Locate every uninfected red blood cell.
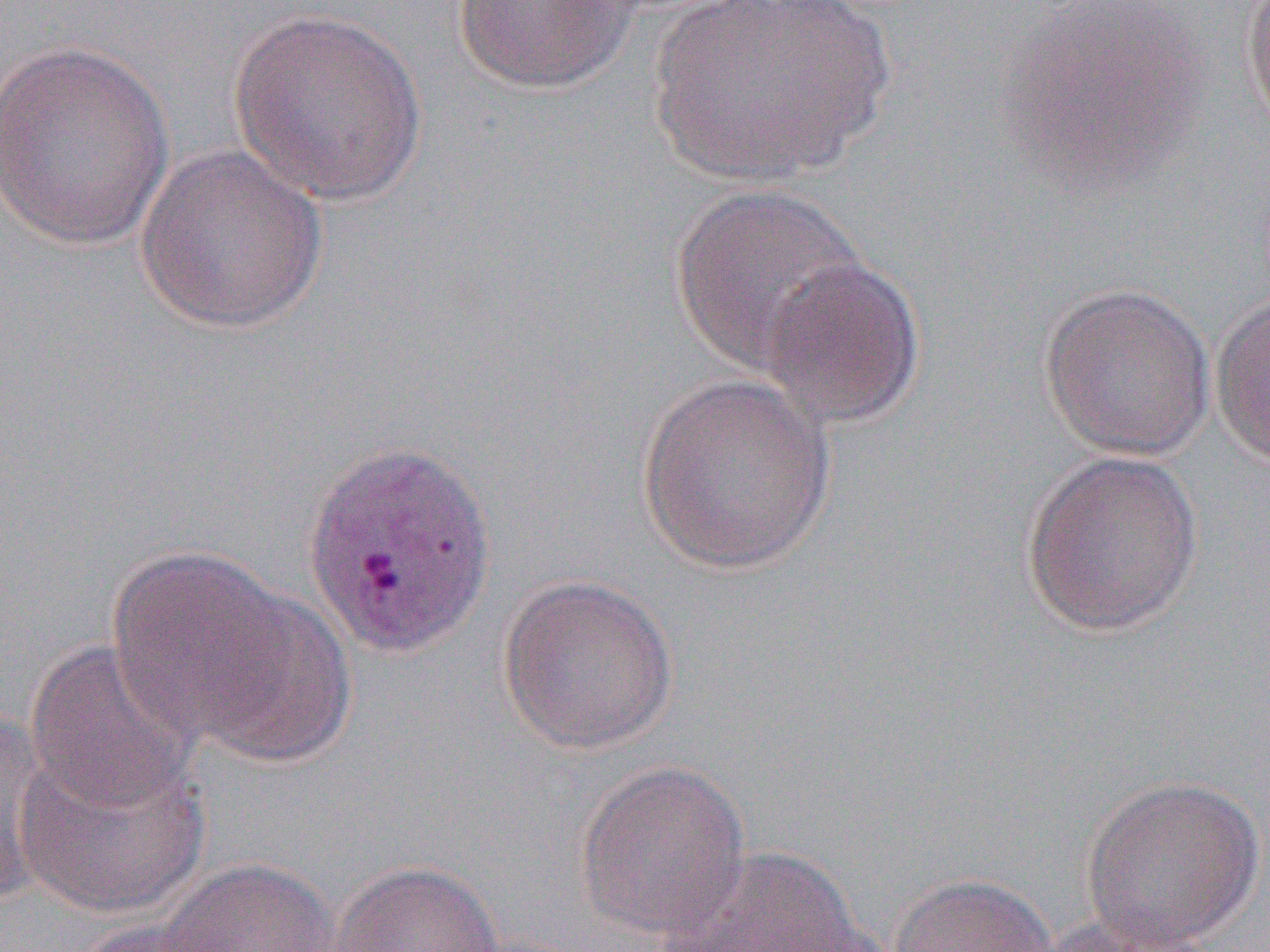
Approximate bounding boxes as (x1,y1)-(x2,y2) corner pairs in pixels.
Uninfected red blood cells: (641,0)-(898,187), (452,1)-(644,95), (1240,1)-(1270,140), (996,3)-(1213,194), (227,7)-(428,208), (0,38)-(176,252), (133,142)-(329,335), (667,183)-(869,375), (758,256)-(926,429), (1038,282)-(1217,462), (1209,291)-(1270,470), (634,374)-(839,575), (1020,450)-(1205,638), (105,545)-(310,752), (496,572)-(680,755), (174,580)-(357,768), (21,639)-(202,815), (0,705)-(58,907), (14,739)-(213,920), (574,759)-(751,941), (1078,774)-(1266,950), (658,846)-(878,952), (158,858)-(344,952), (329,859)-(504,951), (886,871)-(1060,952), (1034,916)-(1219,951), (69,918)-(236,951).

Slide-level diagnosis: Plasmodium vivax. Thin blood film. Image is 1270×952 pixels. Single field of view. Optical microscopy. Captured at 1000x magnification.